State which parasite is depicted.
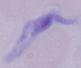
This is a trypanosome.

Photomicrograph. Captured at 1000x magnification.